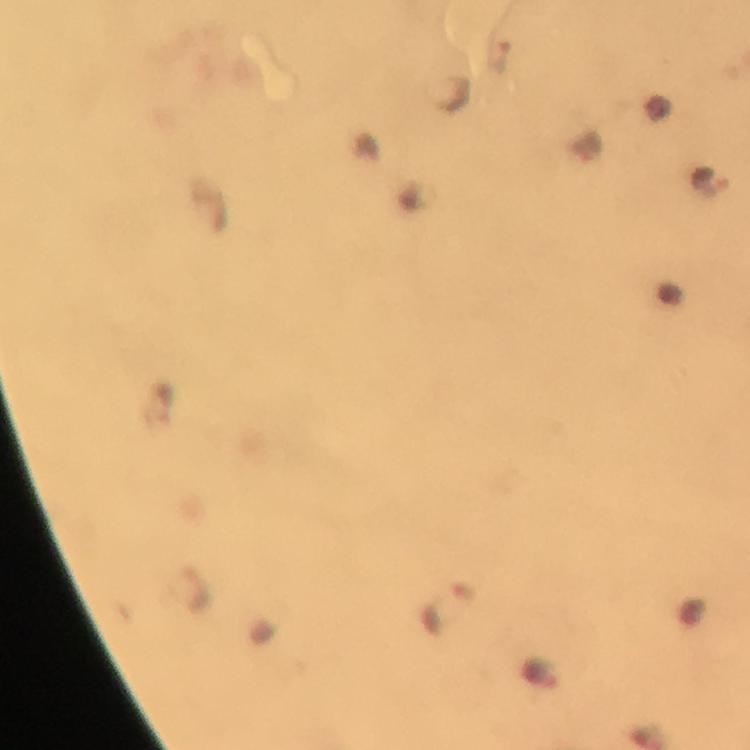

stain: Giemsa
cropped_from: a single field of view
context: from a diagnostic examination for malaria
image_size: 750×750 pixels
plasmodium_parasite_locations: 'approximate centers as (x, y) in pixels: (503, 56), (713, 182), (188, 589), (446, 608), (541, 673)'
capture: smartphone mounted on the microscope
preparation: thick blood film
immersion_oil: applied
magnification: 100x